Name the parasite shown.
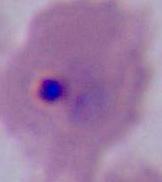

This is Plasmodium.

modality: photomicrograph
magnification: 400x or 1000x